Assess this cell for malaria.
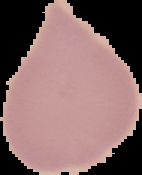
Uninfected.

Summary:
  - Image size: 142×175 pixels
  - Image type: cell region segmented out of the field of view; surrounding area masked to black
  - Preparation: thin blood film